Locate every leukocyte (white blood cell).
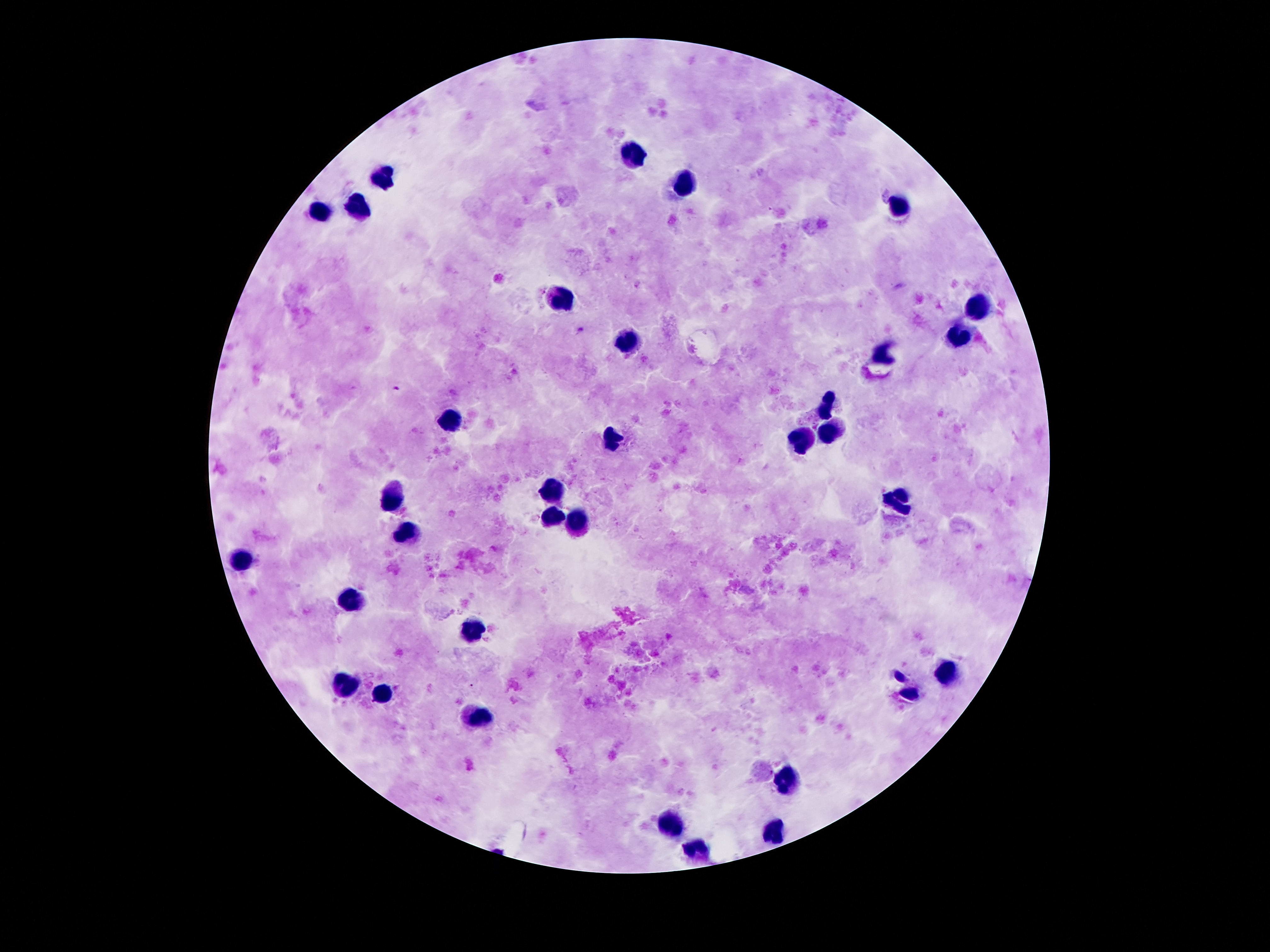

Approximate object centers, in pixels from the top-left corner.
Leukocytes: (x=630, y=156), (x=383, y=177), (x=684, y=186), (x=357, y=207), (x=899, y=207), (x=318, y=212), (x=561, y=294), (x=979, y=305), (x=959, y=339), (x=624, y=345), (x=882, y=354), (x=828, y=404), (x=451, y=417), (x=832, y=425), (x=611, y=438), (x=805, y=440), (x=550, y=490), (x=395, y=498), (x=899, y=503), (x=555, y=513), (x=581, y=520), (x=408, y=535), (x=243, y=561), (x=352, y=598), (x=473, y=628), (x=945, y=673), (x=346, y=684), (x=910, y=692), (x=382, y=694), (x=486, y=712), (x=789, y=776), (x=774, y=826), (x=671, y=828), (x=699, y=852).

capture = smartphone camera through the microscope eyepiece
image size = 1270×952 pixels
preparation = thick blood smear
patient malaria status = not infected
stain = Giemsa
field of view = single
magnification = 100x